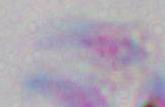

Summary:
  - Identification: Toxoplasma gondii
  - Magnification: 1000x
  - Modality: photomicrograph